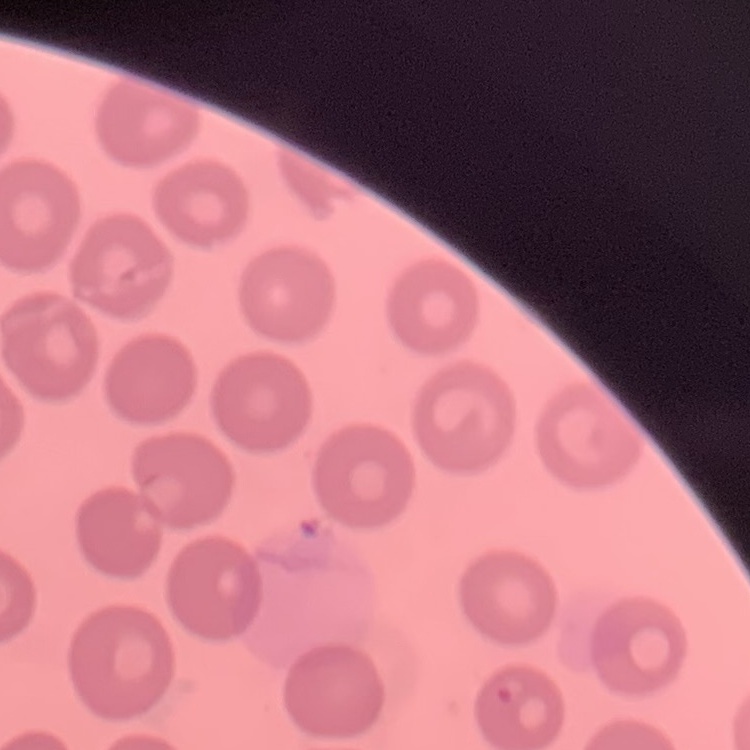
red blood cell morphology = no rouleaux formation
stain = Field's or Giemsa
image type = square crop of a larger photomicrograph
preparation = thin peripheral smear